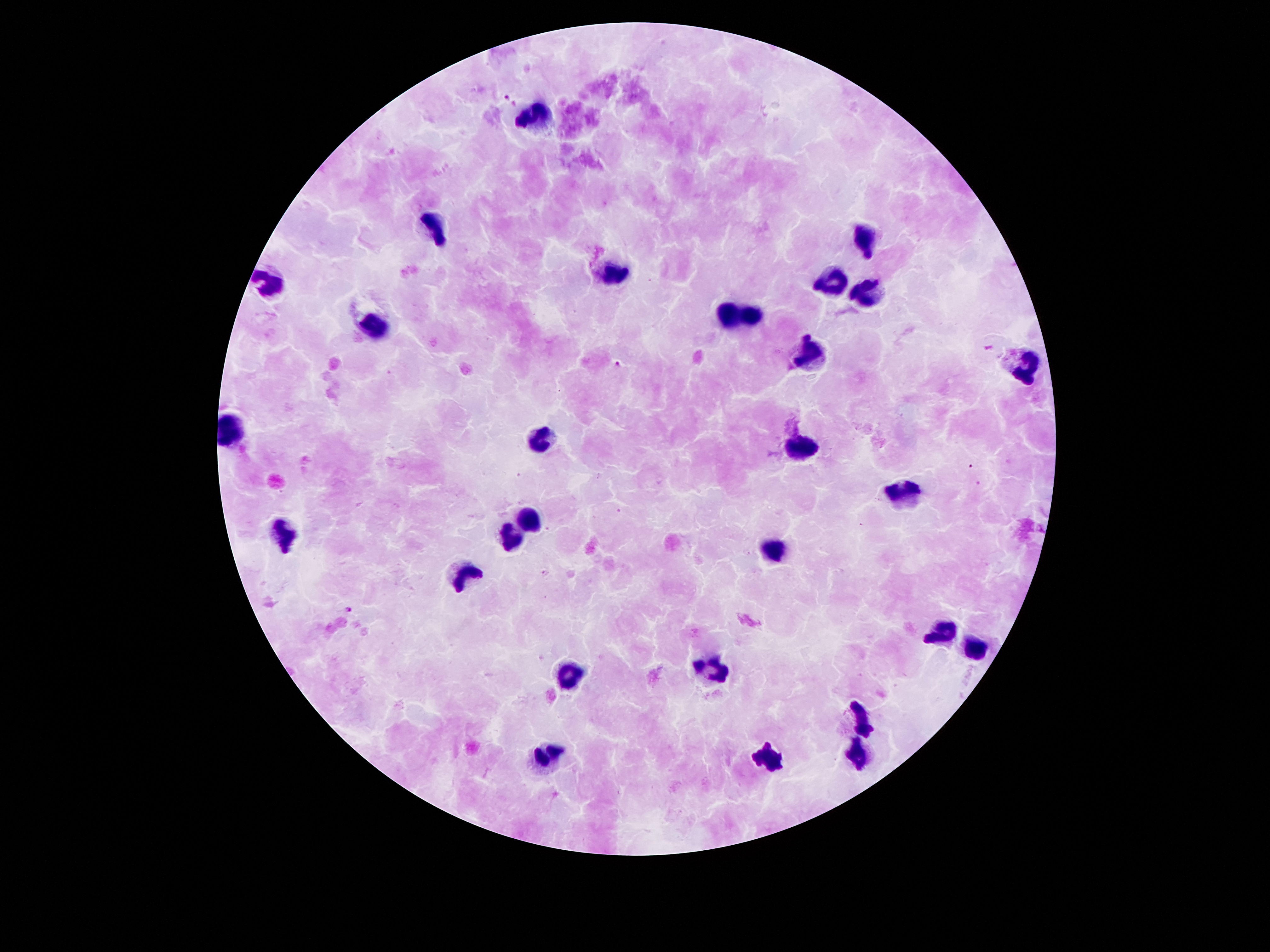 Single field of view. Giemsa stain. Thick blood film. Patient malaria status: positive for Plasmodium falciparum. Photographed through the microscope eyepiece with a smartphone camera. Image is 1270×952 pixels. 100x magnification.